Locate every Plasmodium ovale-infected red blood cell.
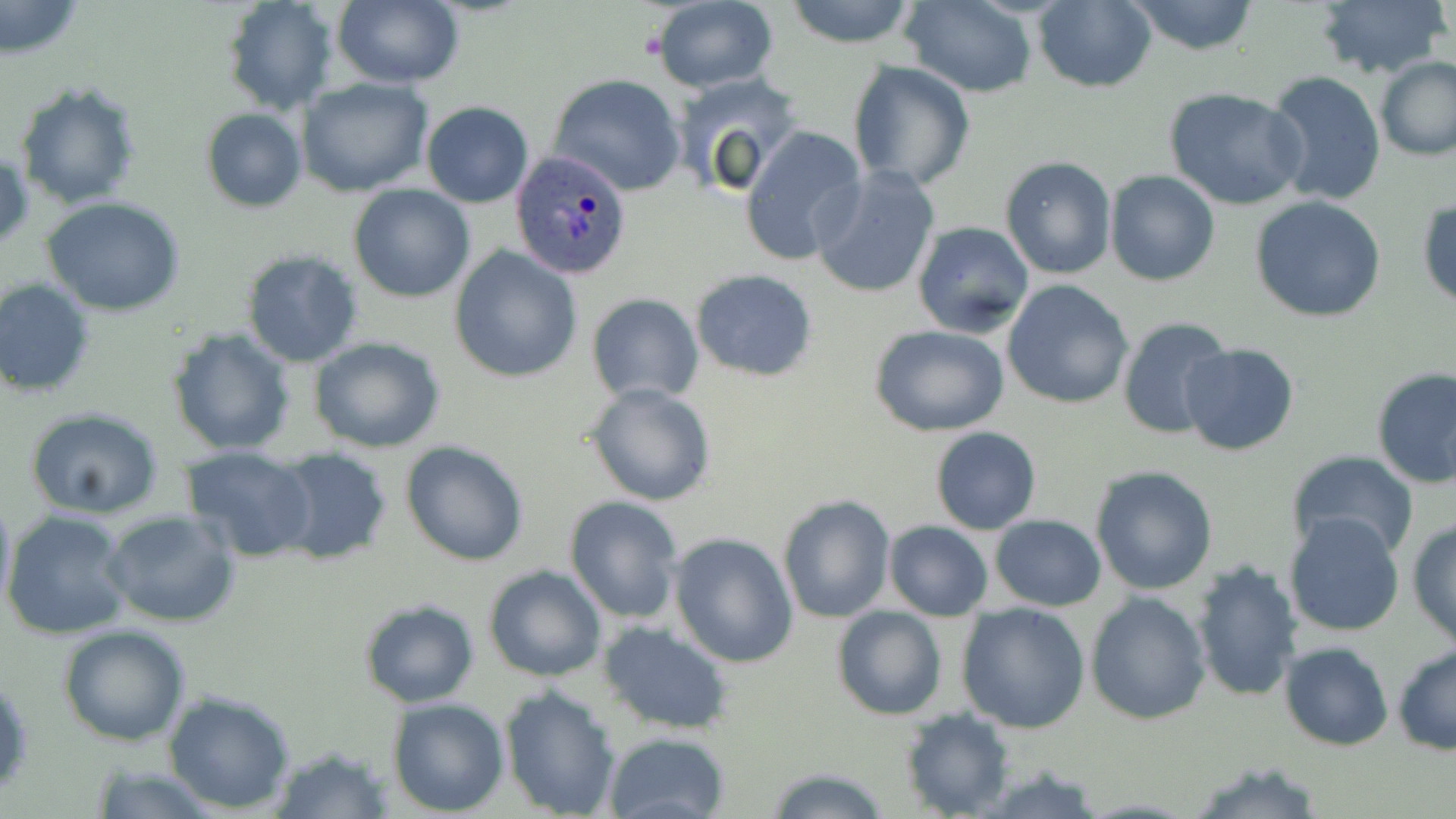

Approximate bounding boxes as [x1, y1, x2, y2] in pixels.
Plasmodium ovale-infected red blood cells: [512, 150, 632, 280].

slide-level diagnosis = Plasmodium ovale
image size = 1456×819 pixels
field of view = single
modality = optical microscopy
magnification = 1000x
stain = May-Grünwald-Giemsa
preparation = thin blood film
uninfected red blood cell locations = approximate bounding boxes as [x1, y1, x2, y2] in pixels: [220, 0, 338, 114], [332, 0, 462, 89], [648, 0, 778, 91], [783, 0, 921, 49], [901, 0, 1038, 96], [1033, 0, 1156, 93], [1313, 0, 1449, 83], [1125, 1, 1260, 54], [1, 2, 85, 58], [1374, 56, 1456, 161], [846, 60, 976, 193], [1266, 70, 1387, 207], [672, 72, 805, 195], [547, 74, 688, 196], [296, 77, 433, 197], [16, 83, 142, 208], [1163, 88, 1308, 212], [422, 102, 532, 207], [201, 109, 306, 212], [739, 124, 867, 265], [1, 150, 33, 254], [1000, 155, 1117, 279], [810, 165, 941, 299], [1104, 170, 1220, 287], [349, 185, 474, 301], [1249, 196, 1389, 322], [1417, 197, 1456, 308], [43, 199, 187, 317], [911, 220, 1033, 337], [449, 245, 584, 383], [241, 249, 364, 368], [690, 269, 818, 381], [0, 278, 96, 398], [1002, 279, 1134, 409], [586, 292, 703, 403], [1116, 316, 1234, 439], [870, 324, 1010, 437], [166, 326, 296, 456], [309, 337, 446, 454], [1179, 343, 1300, 458], [1371, 366, 1456, 490], [584, 382, 717, 506], [25, 407, 165, 518], [930, 427, 1042, 534], [401, 441, 528, 567], [180, 445, 316, 563], [270, 445, 392, 564], [1286, 452, 1421, 561], [1090, 465, 1220, 595], [0, 490, 16, 617], [779, 494, 896, 623], [564, 495, 683, 624], [103, 509, 239, 627], [3, 511, 132, 640], [989, 514, 1106, 611], [1283, 515, 1406, 637], [1407, 516, 1456, 649], [884, 521, 993, 621], [670, 531, 800, 668], [1189, 559, 1305, 703], [482, 564, 607, 682], [1087, 591, 1212, 724], [359, 600, 481, 709], [957, 601, 1090, 734], [831, 606, 947, 719], [598, 620, 734, 735], [59, 625, 190, 746], [1279, 642, 1393, 751], [1392, 643, 1455, 755], [498, 684, 623, 816], [163, 689, 295, 812], [387, 698, 509, 816], [900, 706, 1013, 817], [604, 732, 730, 819], [269, 744, 394, 817], [87, 761, 221, 818], [1186, 762, 1320, 818], [760, 766, 892, 819]